Assess the morphology of the erythrocytes.
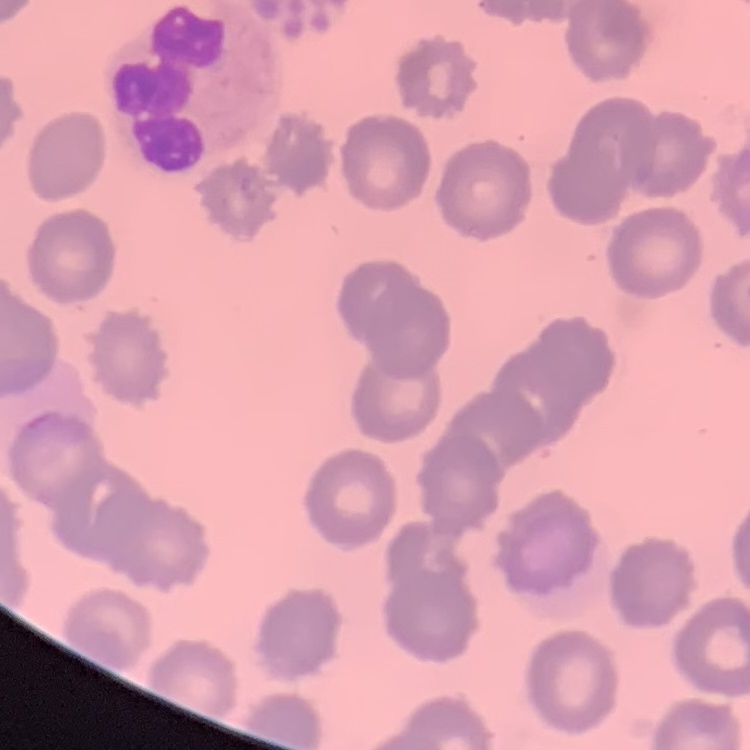

They show no rouleaux formation.

Summary:
  - Preparation: thin blood smear
  - Stain: Field's or Giemsa
  - Image type: one tile cut from a larger photomicrograph